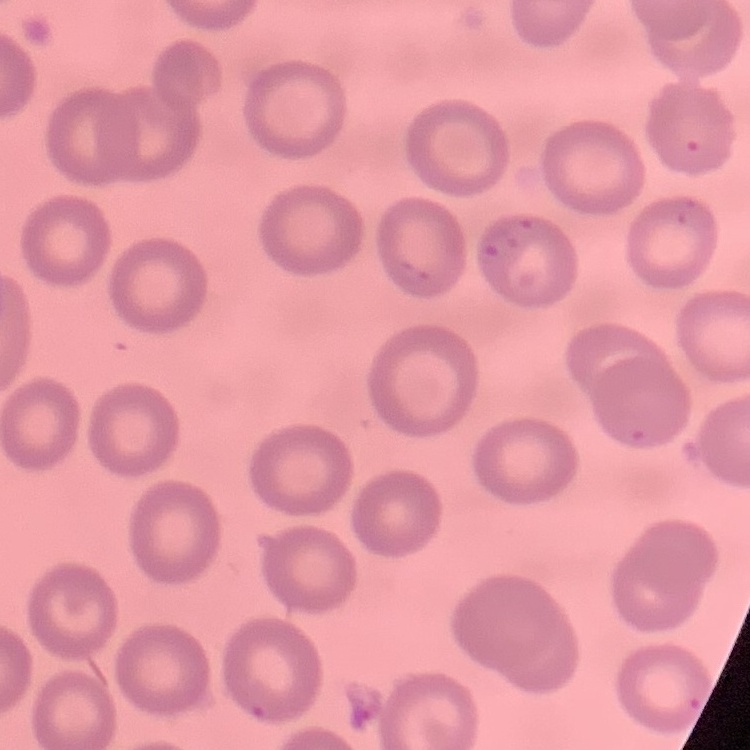
The red blood cells show no rouleaux formation. Square crop of a larger photomicrograph. Field's or Giemsa stain. Thin peripheral smear.